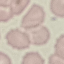
Summary:
  - Result: negative for malaria parasites
  - Capture: smartphone camera at the microscope eyepiece
  - Stain: Giemsa
  - Preparation: thin smear
  - Image type: cell patch, automatically extracted from a larger field of view and resized to 64 × 64 pixels